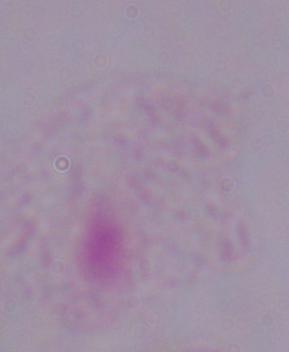

Photomicrograph. A trichomonad is seen. 1000x magnification.